Outline each blood parasite and name the species.
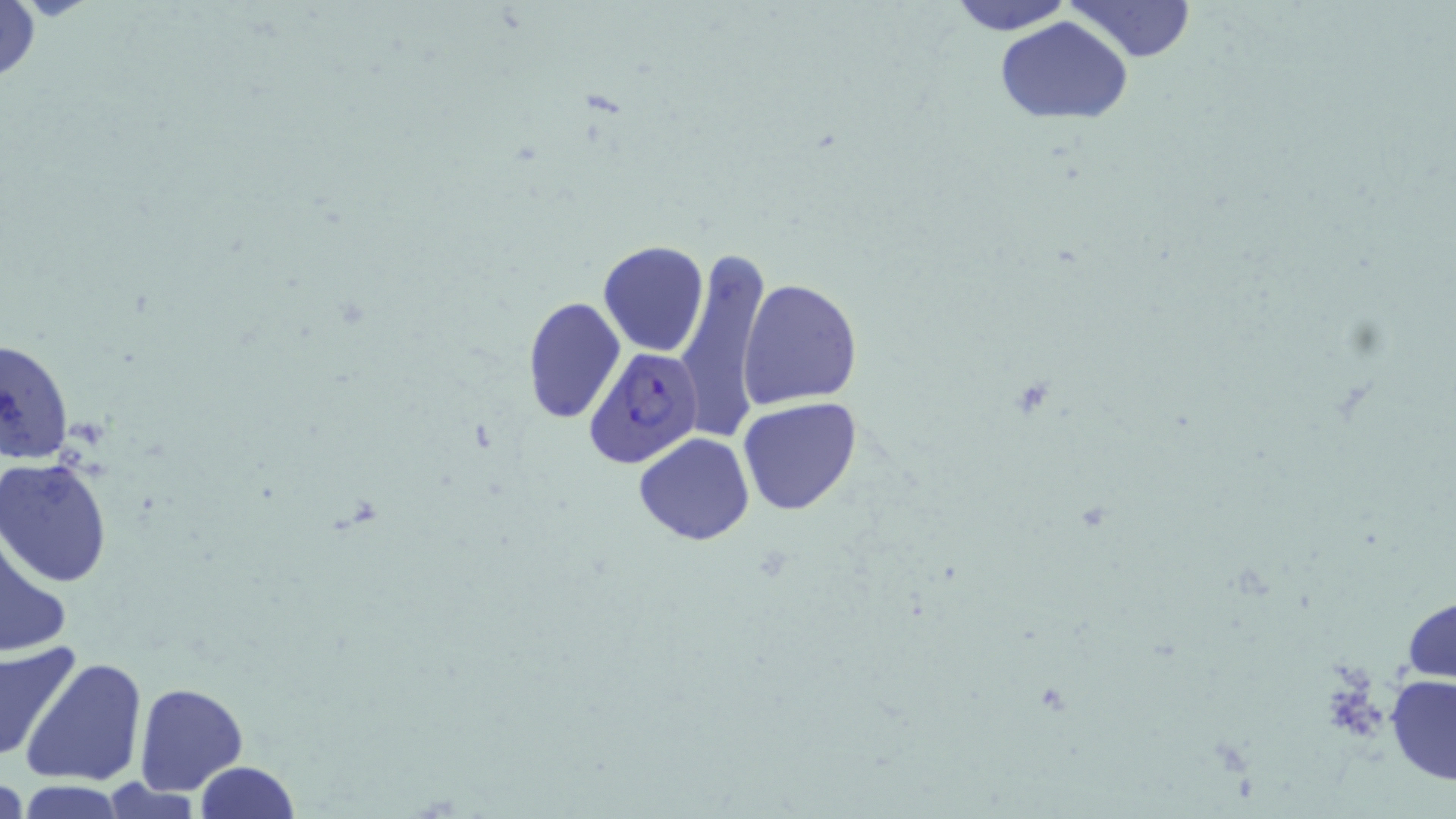

Approximate bounding boxes as (x1,y1)-(x2,y2) corner pairs in pixels.
Plasmodium falciparum-infected red blood cells: (584,346)-(704,470).
No Plasmodium ovale, Plasmodium malariae, Plasmodium vivax, Babesia divergens, or Trypanosoma brucei observed.

Uninfected red blood cell locations: (947,0)-(1075,34), (1067,0)-(1193,63), (1,1)-(42,90), (996,16)-(1134,124), (598,241)-(707,357), (676,246)-(774,442), (739,277)-(862,408), (522,297)-(625,424), (0,333)-(74,466), (737,398)-(863,516), (633,432)-(756,545), (0,456)-(113,585), (1,534)-(71,661), (1402,594)-(1455,686), (0,637)-(82,765), (21,655)-(148,788), (1386,674)-(1456,784), (134,683)-(248,795), (194,761)-(300,819), (1,772)-(25,819), (97,778)-(203,819), (14,780)-(126,818). Slide-level diagnosis: Plasmodium falciparum. 1000x magnification. Single field of view. Optical microscopy. May-Grünwald-Giemsa stain. Image is 1456×819 pixels. Thin blood smear.